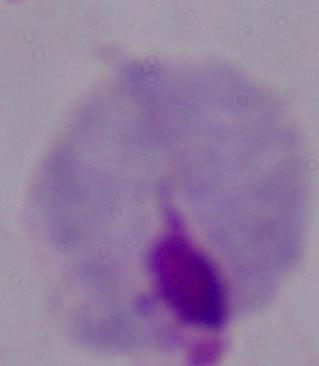
identification = trichomonad
magnification = 1000x
modality = micrograph